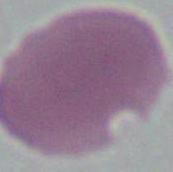

Summary:
  - Identification: erythrocyte
  - Modality: micrograph
  - Magnification: 1000x